Identify the parasite.
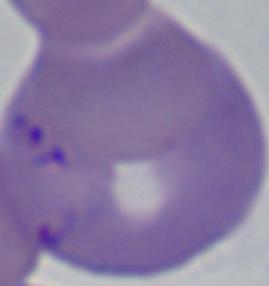

Babesia.

{
  "modality": "micrograph",
  "magnification": "1000x"
}